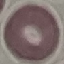

Summary:
  - Malaria status: uninfected
  - Image type: cell patch, automatically extracted from a larger field of view and resized to 64 × 64 pixels
  - Stain: Giemsa
  - Preparation: thin smear
  - Capture: smartphone through the microscope eyepiece